Comment on the morphology of the red blood cells.
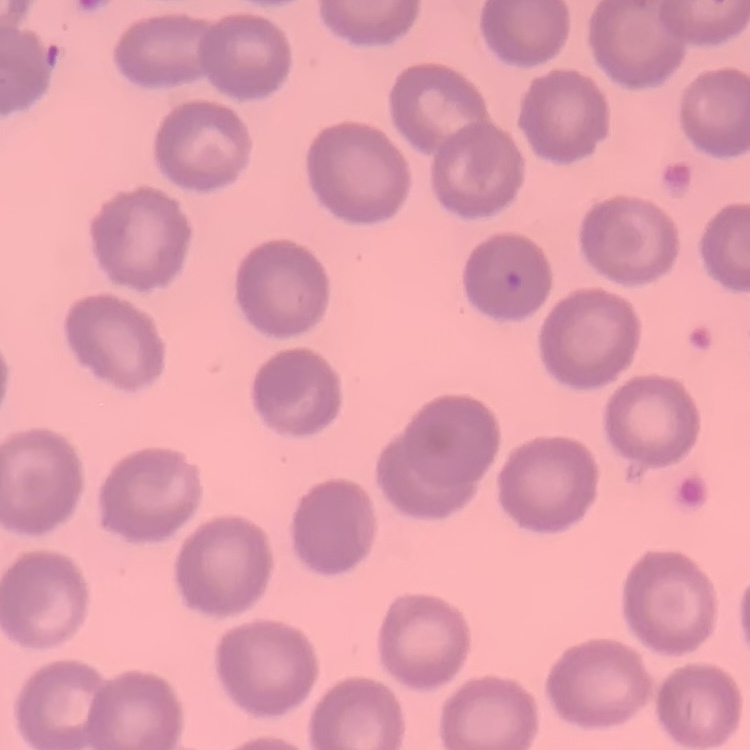

They show no rouleaux formation.

Summary:
  - Stain: Field's or Giemsa
  - Preparation: thin blood smear
  - Image type: square crop of a larger photomicrograph